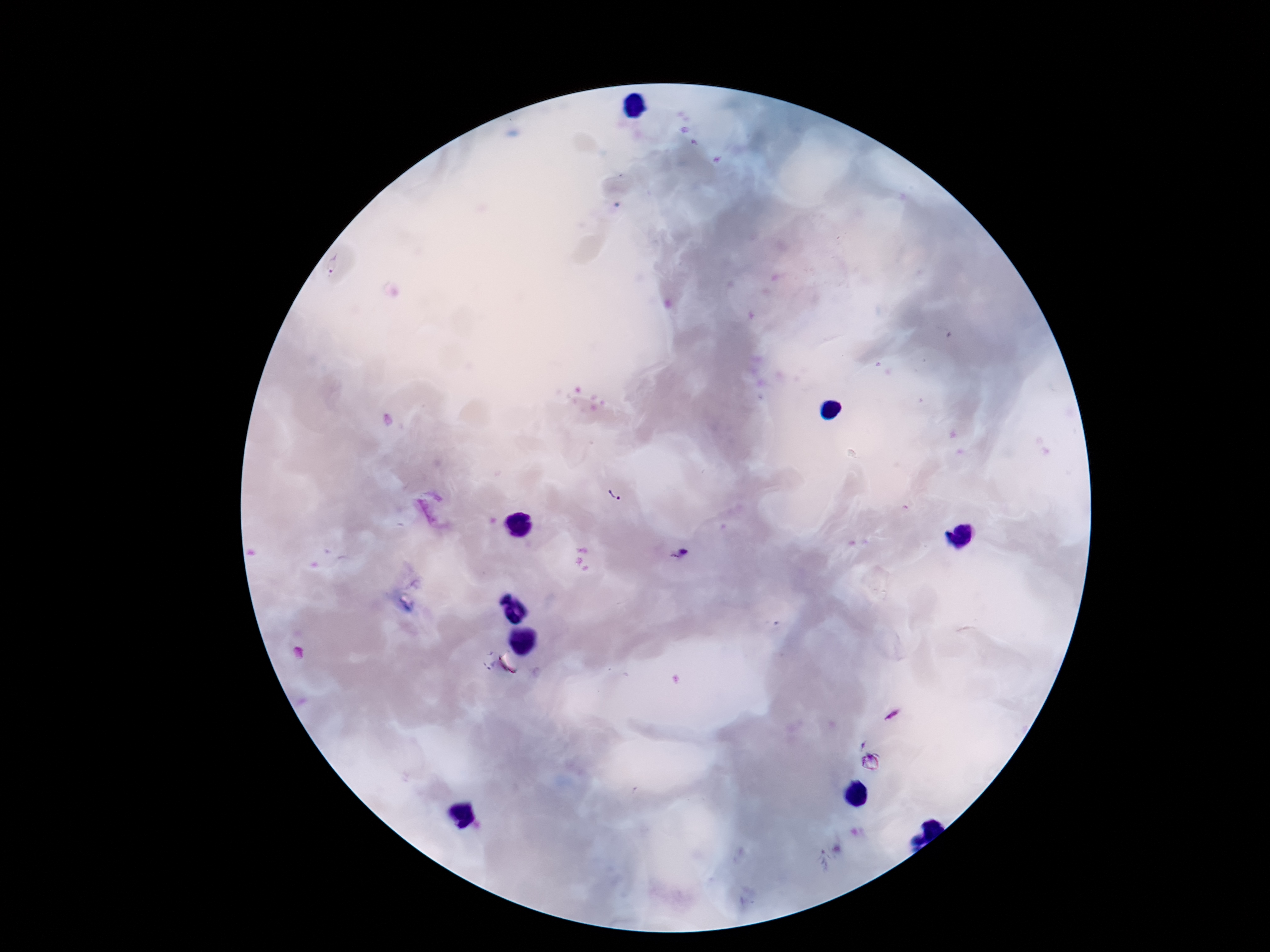
Approximate object centers, in pixels from the top-left corner. Plasmodium parasite locations: (x=332, y=266), (x=613, y=497), (x=678, y=553), (x=825, y=861). Image is 1270×952 pixels. Single field of view. Thick peripheral-blood smear. 100x magnification. Photographed through the microscope eyepiece with a smartphone camera. Giemsa-stained preparation. Patient malaria status: infected.